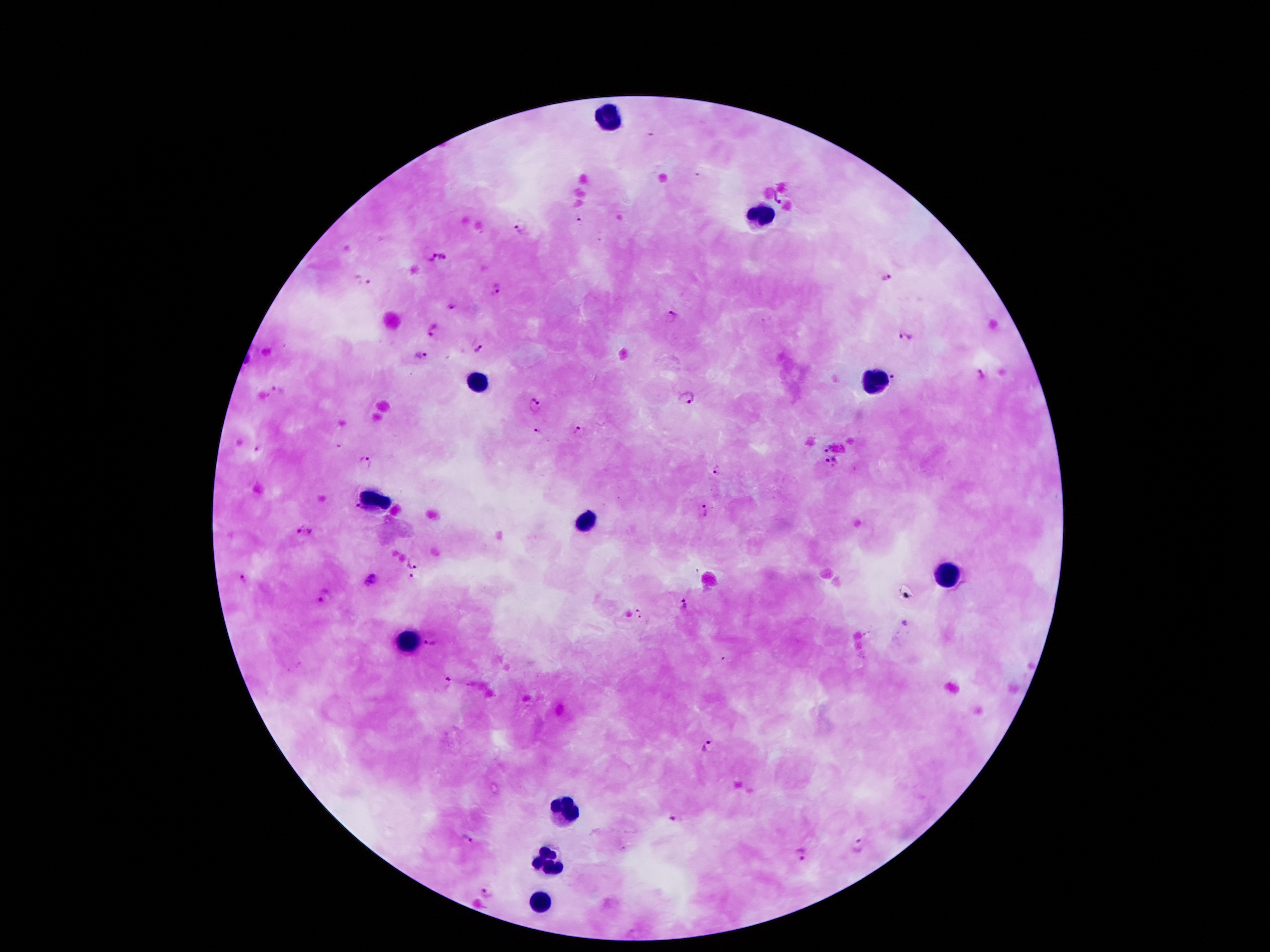

Approximate centers as (x, y) in pixels. Plasmodium parasite locations: (777, 199), (576, 219), (521, 226), (431, 257), (444, 258), (889, 277), (363, 281), (496, 289), (450, 306), (670, 317), (431, 330), (905, 338), (478, 349), (421, 354), (895, 374), (981, 374), (277, 390), (687, 399), (535, 406), (538, 432), (581, 432), (827, 447), (258, 449), (829, 461), (365, 462), (716, 473), (355, 506), (704, 512), (302, 533), (414, 560), (243, 579), (412, 579), (372, 580), (325, 596), (684, 603), (639, 614), (429, 644), (446, 678), (707, 746), (673, 821), (467, 839), (859, 847), (801, 853), (486, 890). Leukocyte locations: (608, 116), (760, 214), (872, 380), (476, 382), (376, 502), (586, 518), (947, 576), (410, 644), (562, 812), (546, 856), (540, 898). Thick peripheral-blood smear. Image is 1270×952 pixels. Smartphone photograph taken through the microscope eyepiece. Patient malaria status: infected with Plasmodium falciparum. Single field of view. Giemsa stain. 100x magnification.